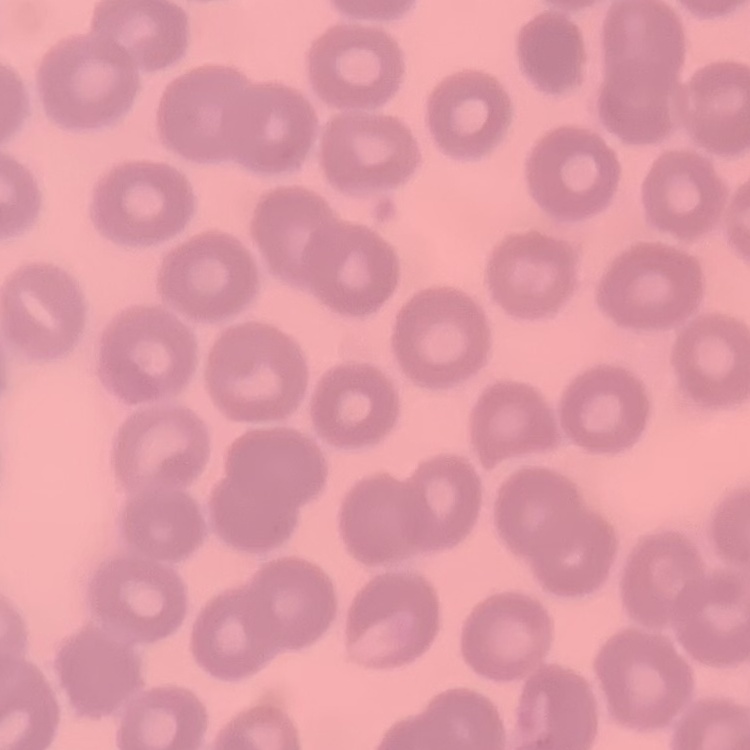

{
  "erythrocyte_morphology": "no rouleaux formation",
  "image_type": "square crop of a larger photomicrograph",
  "stain": "Field's or Giemsa",
  "preparation": "thin blood film"
}